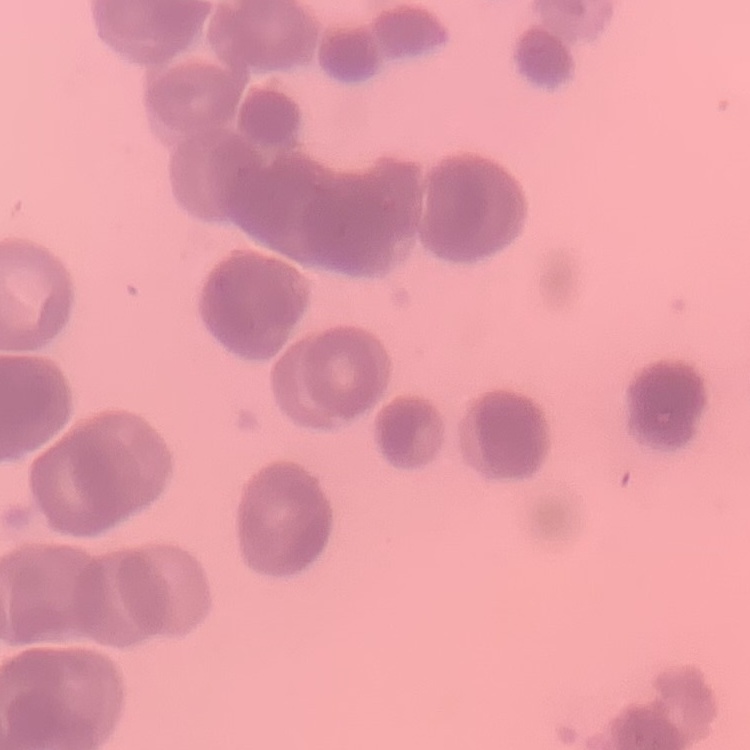
Summary:
  - Erythrocyte morphology: rouleaux formation
  - Stain: Field's or Giemsa
  - Image type: one tile cut from a larger photomicrograph
  - Preparation: thin blood smear